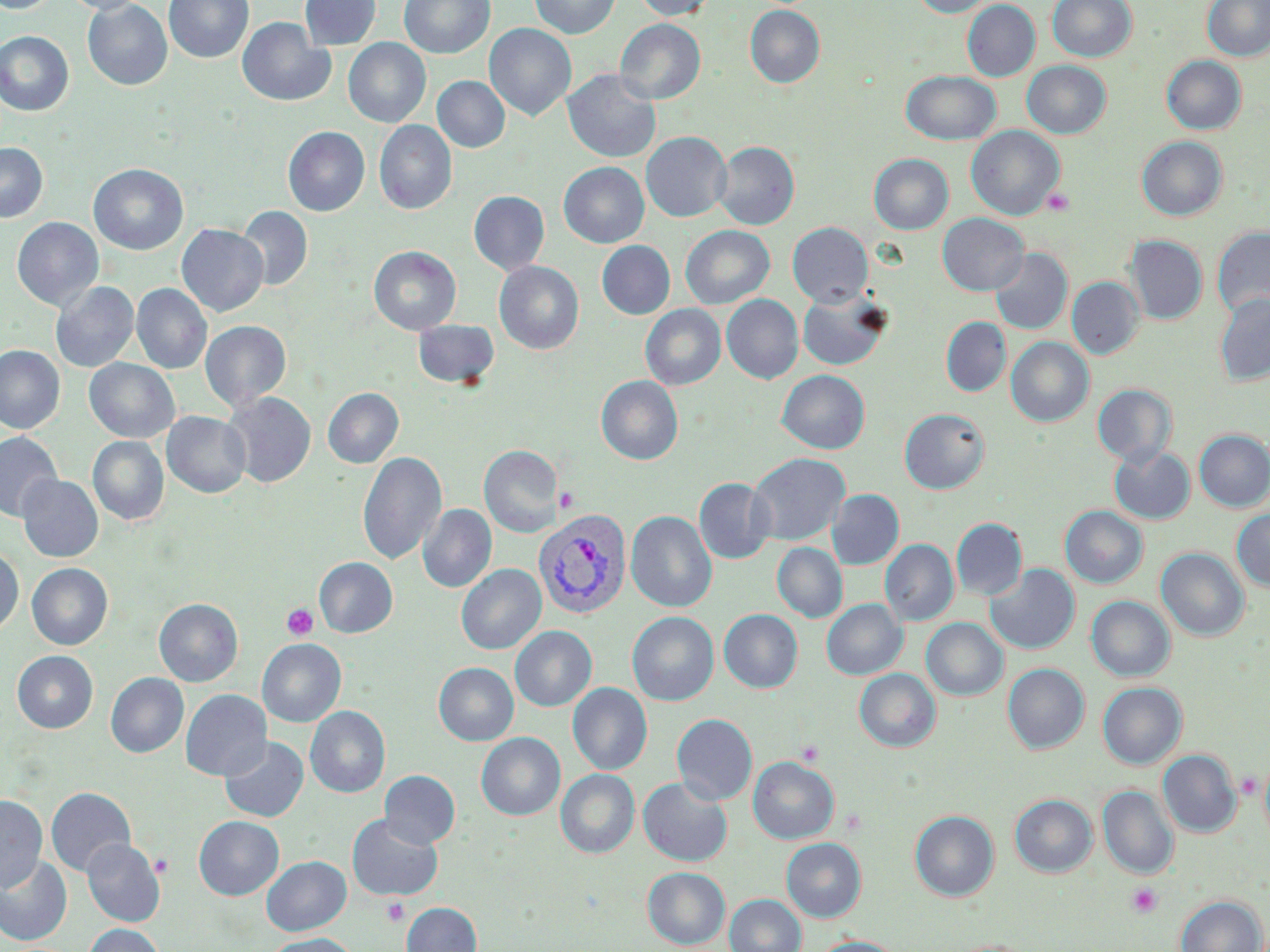

Approximate bounding boxes as named x1/y1/x2/y2 corners in pixels. Platelet locations: (x1=1042, y1=188, x2=1075, y2=216), (x1=554, y1=487, x2=580, y2=514), (x1=282, y1=604, x2=318, y2=641), (x1=796, y1=740, x2=824, y2=766), (x1=840, y1=808, x2=868, y2=835), (x1=1126, y1=883, x2=1163, y2=918), (x1=381, y1=898, x2=410, y2=926). Uninfected red blood cell locations: (x1=0, y1=0, x2=59, y2=14), (x1=61, y1=0, x2=147, y2=15), (x1=163, y1=0, x2=254, y2=64), (x1=299, y1=0, x2=381, y2=50), (x1=399, y1=0, x2=494, y2=59), (x1=529, y1=0, x2=620, y2=39), (x1=632, y1=0, x2=716, y2=20), (x1=912, y1=0, x2=993, y2=17), (x1=1047, y1=0, x2=1136, y2=62), (x1=1202, y1=0, x2=1270, y2=61), (x1=83, y1=1, x2=172, y2=90), (x1=962, y1=1, x2=1040, y2=81), (x1=745, y1=5, x2=825, y2=88), (x1=1192, y1=6, x2=1268, y2=108), (x1=238, y1=18, x2=335, y2=107), (x1=615, y1=19, x2=705, y2=105), (x1=484, y1=23, x2=576, y2=122), (x1=0, y1=31, x2=74, y2=116), (x1=343, y1=38, x2=431, y2=128), (x1=1162, y1=55, x2=1246, y2=134), (x1=1021, y1=60, x2=1111, y2=138), (x1=562, y1=69, x2=661, y2=163), (x1=901, y1=70, x2=1000, y2=145), (x1=432, y1=76, x2=510, y2=153), (x1=375, y1=120, x2=457, y2=216), (x1=966, y1=125, x2=1065, y2=220), (x1=283, y1=126, x2=370, y2=216), (x1=641, y1=132, x2=731, y2=222), (x1=1137, y1=136, x2=1227, y2=221), (x1=714, y1=141, x2=800, y2=230), (x1=0, y1=142, x2=48, y2=223), (x1=869, y1=154, x2=953, y2=234), (x1=558, y1=162, x2=649, y2=248), (x1=89, y1=164, x2=189, y2=255), (x1=468, y1=191, x2=549, y2=275), (x1=236, y1=205, x2=313, y2=291), (x1=937, y1=213, x2=1029, y2=295), (x1=12, y1=217, x2=104, y2=313), (x1=788, y1=222, x2=873, y2=307), (x1=177, y1=224, x2=268, y2=317), (x1=680, y1=225, x2=774, y2=308), (x1=1211, y1=226, x2=1270, y2=320), (x1=1124, y1=235, x2=1208, y2=324), (x1=597, y1=241, x2=675, y2=319), (x1=369, y1=246, x2=461, y2=335), (x1=989, y1=248, x2=1072, y2=334), (x1=494, y1=261, x2=584, y2=355), (x1=1067, y1=276, x2=1145, y2=359), (x1=50, y1=281, x2=139, y2=373), (x1=132, y1=283, x2=212, y2=375), (x1=797, y1=289, x2=892, y2=370), (x1=1214, y1=294, x2=1270, y2=386), (x1=722, y1=295, x2=803, y2=384), (x1=640, y1=304, x2=726, y2=390), (x1=941, y1=317, x2=1011, y2=396), (x1=201, y1=320, x2=291, y2=412), (x1=413, y1=320, x2=499, y2=389), (x1=1006, y1=337, x2=1094, y2=427), (x1=0, y1=345, x2=64, y2=434), (x1=84, y1=358, x2=179, y2=443), (x1=777, y1=369, x2=870, y2=453), (x1=596, y1=376, x2=683, y2=464), (x1=1092, y1=384, x2=1176, y2=465), (x1=323, y1=388, x2=403, y2=468), (x1=223, y1=392, x2=316, y2=489), (x1=899, y1=408, x2=990, y2=493), (x1=162, y1=411, x2=251, y2=499), (x1=1194, y1=429, x2=1270, y2=511), (x1=0, y1=431, x2=63, y2=522), (x1=88, y1=436, x2=169, y2=527), (x1=479, y1=445, x2=564, y2=537), (x1=1109, y1=445, x2=1195, y2=524), (x1=358, y1=451, x2=446, y2=566), (x1=747, y1=453, x2=850, y2=545), (x1=17, y1=474, x2=103, y2=562), (x1=694, y1=477, x2=775, y2=563), (x1=827, y1=489, x2=904, y2=569), (x1=418, y1=504, x2=496, y2=592), (x1=1060, y1=506, x2=1148, y2=588), (x1=1231, y1=508, x2=1270, y2=591), (x1=626, y1=510, x2=717, y2=612), (x1=951, y1=518, x2=1027, y2=600), (x1=880, y1=539, x2=958, y2=626), (x1=772, y1=543, x2=847, y2=622), (x1=0, y1=546, x2=23, y2=637), (x1=1156, y1=547, x2=1249, y2=641), (x1=314, y1=557, x2=397, y2=637), (x1=27, y1=563, x2=113, y2=651), (x1=456, y1=564, x2=546, y2=655), (x1=985, y1=564, x2=1080, y2=654), (x1=1086, y1=596, x2=1175, y2=681), (x1=154, y1=598, x2=243, y2=687), (x1=822, y1=599, x2=907, y2=679), (x1=719, y1=609, x2=802, y2=693), (x1=627, y1=612, x2=718, y2=705), (x1=921, y1=618, x2=1008, y2=700), (x1=510, y1=626, x2=597, y2=711), (x1=257, y1=639, x2=346, y2=727), (x1=12, y1=651, x2=98, y2=733), (x1=433, y1=663, x2=518, y2=745), (x1=1003, y1=663, x2=1089, y2=753), (x1=854, y1=668, x2=940, y2=751), (x1=106, y1=672, x2=189, y2=758), (x1=1097, y1=682, x2=1187, y2=769), (x1=568, y1=683, x2=652, y2=775), (x1=181, y1=689, x2=271, y2=781), (x1=305, y1=706, x2=390, y2=798), (x1=672, y1=713, x2=757, y2=804), (x1=476, y1=733, x2=565, y2=820), (x1=219, y1=736, x2=309, y2=823), (x1=1158, y1=749, x2=1242, y2=837), (x1=1260, y1=755, x2=1270, y2=848), (x1=748, y1=756, x2=839, y2=844), (x1=555, y1=769, x2=639, y2=858), (x1=380, y1=770, x2=460, y2=848), (x1=638, y1=777, x2=732, y2=866), (x1=1097, y1=785, x2=1179, y2=879), (x1=46, y1=786, x2=136, y2=877), (x1=0, y1=794, x2=47, y2=892), (x1=1010, y1=794, x2=1097, y2=877), (x1=910, y1=810, x2=999, y2=901), (x1=346, y1=814, x2=444, y2=900), (x1=194, y1=816, x2=284, y2=900), (x1=81, y1=838, x2=165, y2=926), (x1=781, y1=838, x2=866, y2=922), (x1=0, y1=853, x2=72, y2=945), (x1=262, y1=856, x2=351, y2=935), (x1=642, y1=867, x2=730, y2=949), (x1=725, y1=894, x2=806, y2=952), (x1=1176, y1=895, x2=1265, y2=952), (x1=402, y1=902, x2=481, y2=952), (x1=83, y1=924, x2=164, y2=952), (x1=265, y1=934, x2=357, y2=952), (x1=812, y1=936, x2=904, y2=952), (x1=947, y1=940, x2=1038, y2=952). Plasmodium vivax-infected red blood cell locations: (x1=533, y1=508, x2=632, y2=620). Slide-level diagnosis: Plasmodium vivax. Image is 1270×952 pixels. Thin blood film. Single field of view. Captured at 1000x magnification. May-Grünwald-Giemsa stain. Optical microscopy.